Locate Plasmodium parasites and leukocytes.
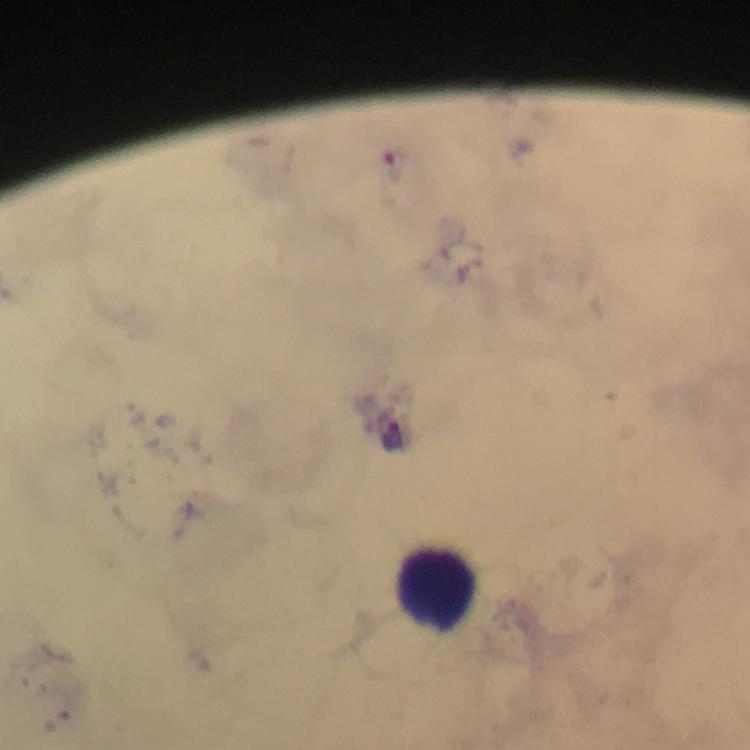

Approximate centers as {x, y} in pixels.
Plasmodium parasites: {395, 160}, {393, 435}.
Leukocytes: {437, 588}.

Summary:
  - Magnification: 100x
  - Preparation: thick smear
  - Context: from a malaria diagnostic workup
  - Stain: Giemsa
  - Immersion oil: used
  - Image size: 750×750 pixels
  - Capture: smartphone camera through the microscope
  - Cropped from: a single field of view